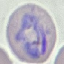
Summary:
  - Malaria status: parasitized
  - Capture: smartphone through the microscope eyepiece
  - Image type: automatically extracted cell patch, resized to 64 × 64 pixels
  - Preparation: thin blood film
  - Stain: Giemsa